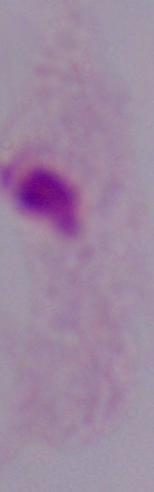
Summary:
  - Modality: micrograph
  - Identification: trichomonad
  - Magnification: 1000x